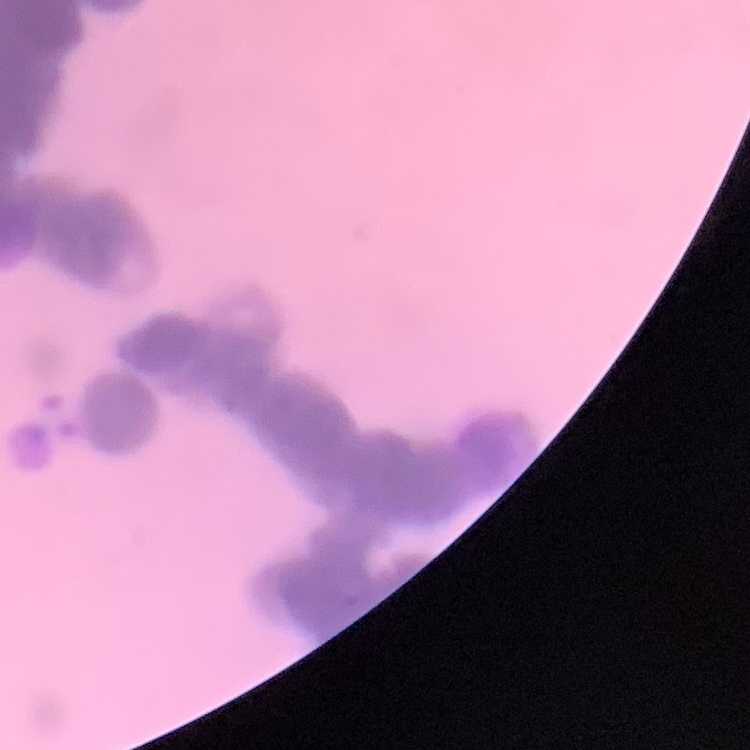
Summary:
  - Erythrocyte morphology: rouleaux formation
  - Stain: Field's or Giemsa
  - Image type: square crop of a larger photomicrograph
  - Preparation: thin peripheral smear